Outline each blood parasite and name the species.
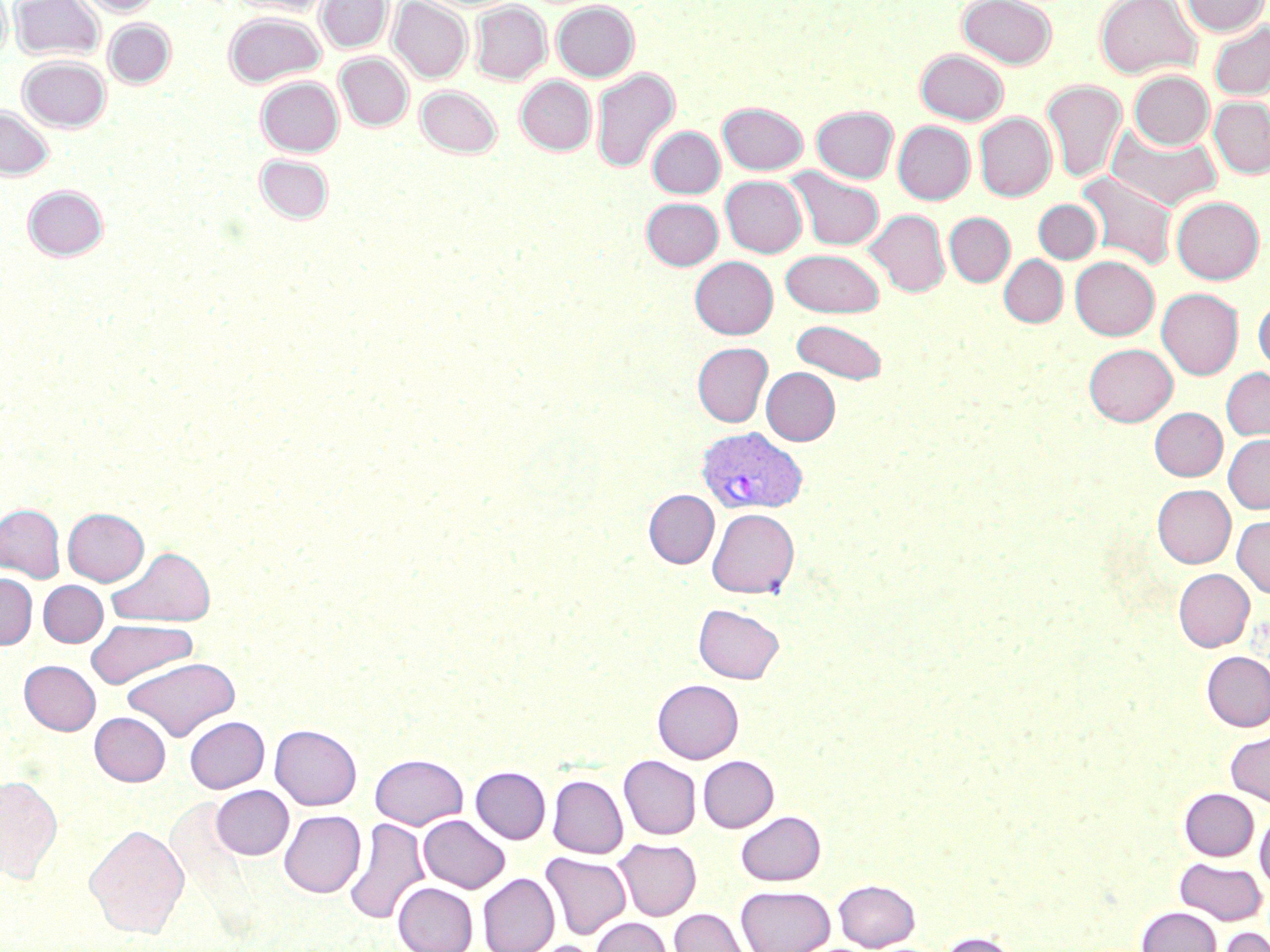

Approximate bounding boxes as (x1,y1)-(x2,y2) corner pairs in pixels.
Plasmodium vivax-infected red blood cells: (695,426)-(808,515).
No Plasmodium falciparum, Plasmodium ovale, Plasmodium malariae, Babesia divergens, or Trypanosoma brucei observed.

{
  "slide_level_diagnosis": "Plasmodium vivax",
  "magnification": "1000x",
  "field_of_view": "one of a larger specimen",
  "image_size": "1270×952 pixels",
  "preparation": "thin blood film",
  "uninfected_red_blood_cell_locations": "approximate bounding boxes as (x1,y1)-(x2,y2) corner pairs in pixels: (0,0)-(11,63), (10,0)-(103,61), (78,0)-(161,16), (229,0)-(331,16), (316,0)-(392,53), (389,0)-(471,82), (957,0)-(1057,68), (1094,0)-(1201,79), (1181,0)-(1269,36), (470,1)-(551,84), (552,1)-(639,81), (224,12)-(325,87), (104,19)-(175,88), (1209,21)-(1270,100), (915,49)-(1009,124), (335,53)-(413,131), (18,55)-(111,132), (591,67)-(680,174), (1128,70)-(1214,150), (256,76)-(343,156), (516,76)-(596,155), (1041,80)-(1127,183), (416,86)-(502,157), (1209,97)-(1270,178), (718,103)-(807,174), (0,105)-(54,180), (812,106)-(898,183), (974,112)-(1056,200), (893,121)-(975,204), (1107,125)-(1221,210), (647,126)-(725,199), (255,154)-(334,225), (788,168)-(884,250), (1077,171)-(1178,270), (720,175)-(807,257), (23,185)-(108,261), (1171,196)-(1265,284), (641,197)-(723,270), (1034,199)-(1101,263), (865,209)-(950,296), (944,212)-(1015,286), (780,248)-(885,317), (999,255)-(1067,327), (690,256)-(778,339), (1070,256)-(1159,340), (1157,288)-(1243,379), (1253,299)-(1270,374), (791,319)-(887,384), (692,342)-(773,427), (1084,343)-(1177,426), (761,367)-(840,445), (1221,367)-(1270,441), (1150,407)-(1227,481), (1223,434)-(1270,513), (1152,484)-(1235,568), (644,490)-(719,568), (0,504)-(65,582), (63,507)-(149,585), (707,508)-(799,598), (1232,515)-(1270,598), (109,546)-(216,627), (1173,569)-(1254,651), (0,572)-(37,649), (38,580)-(108,647), (693,603)-(784,684), (86,619)-(197,688), (1201,651)-(1270,731), (122,657)-(240,741), (20,660)-(100,735), (652,679)-(743,763), (90,712)-(171,786), (185,716)-(269,793), (270,724)-(361,810), (1225,730)-(1270,808), (370,754)-(468,830), (698,755)-(779,832), (619,756)-(701,839), (471,766)-(551,843), (0,774)-(63,883), (548,775)-(628,858), (210,785)-(293,860), (1179,788)-(1258,860), (279,810)-(365,897), (736,810)-(826,885), (1254,810)-(1270,894), (418,815)-(509,893), (343,818)-(430,925), (84,824)-(189,938), (612,837)-(700,921), (541,853)-(631,939), (1174,858)-(1267,925), (478,873)-(559,952), (834,879)-(920,951), (393,882)-(478,952), (735,885)-(835,952), (1137,906)-(1221,952), (669,908)-(751,952), (591,917)-(671,952), (1217,927)-(1270,952), (937,931)-(1022,952), (526,940)-(605,952)",
  "modality": "optical microscopy",
  "stain": "May-Grünwald-Giemsa"
}